Give the preparation type.
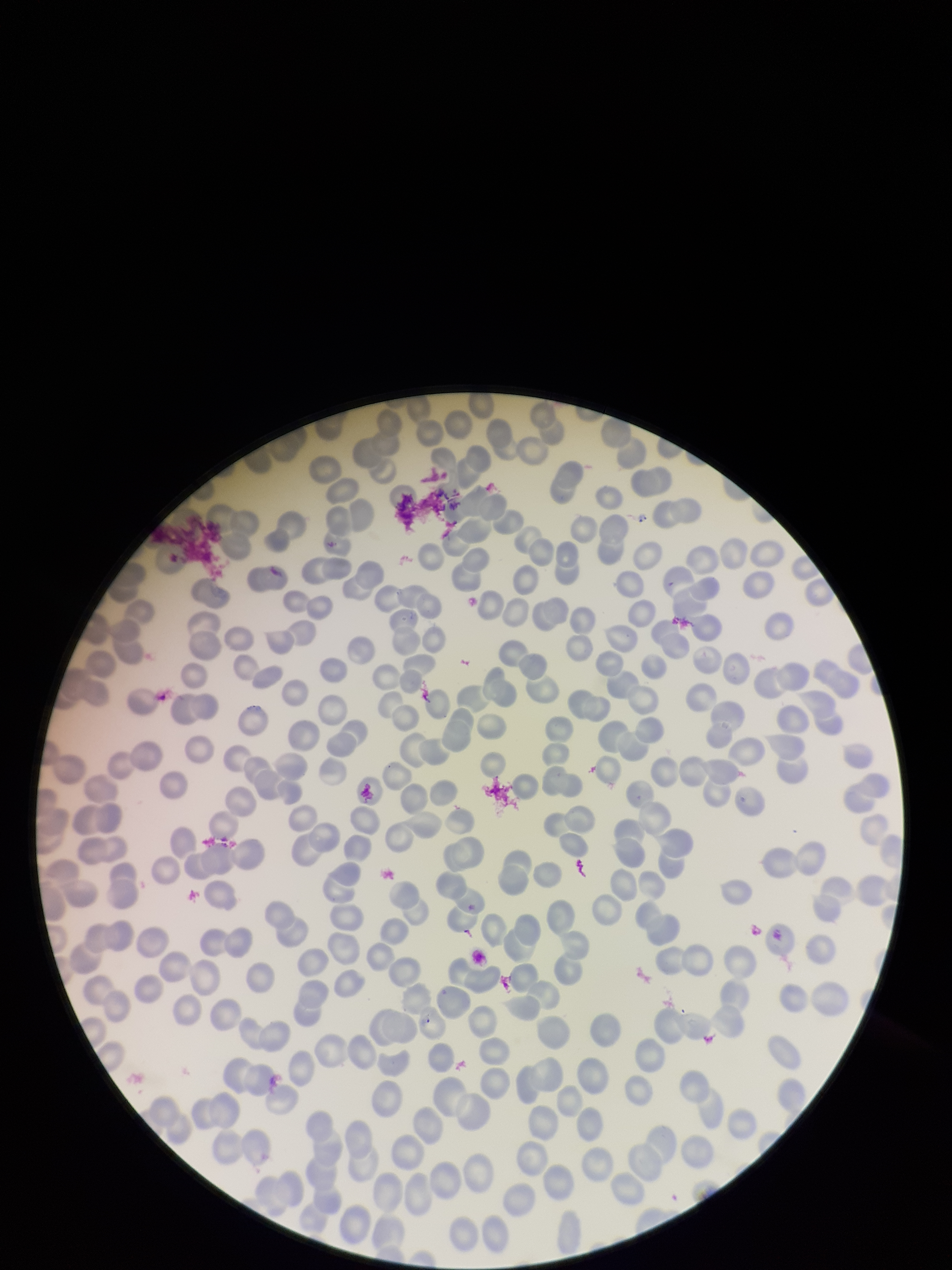
It is a thin blood smear.

image size = 952×1270 pixels
field of view = single
red blood cell count = 248
capture = smartphone photograph through the microscope eyepiece
parasitized red blood cell count = 0
parasitized red blood cells = none detected
stain = Giemsa
patient malaria status = negative